Name the parasite shown.
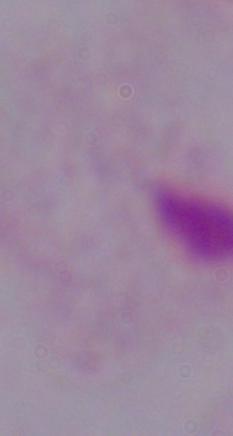
This is a trichomonad.

magnification = 1000x
modality = photomicrograph